Locate every blood parasite and identify its species.
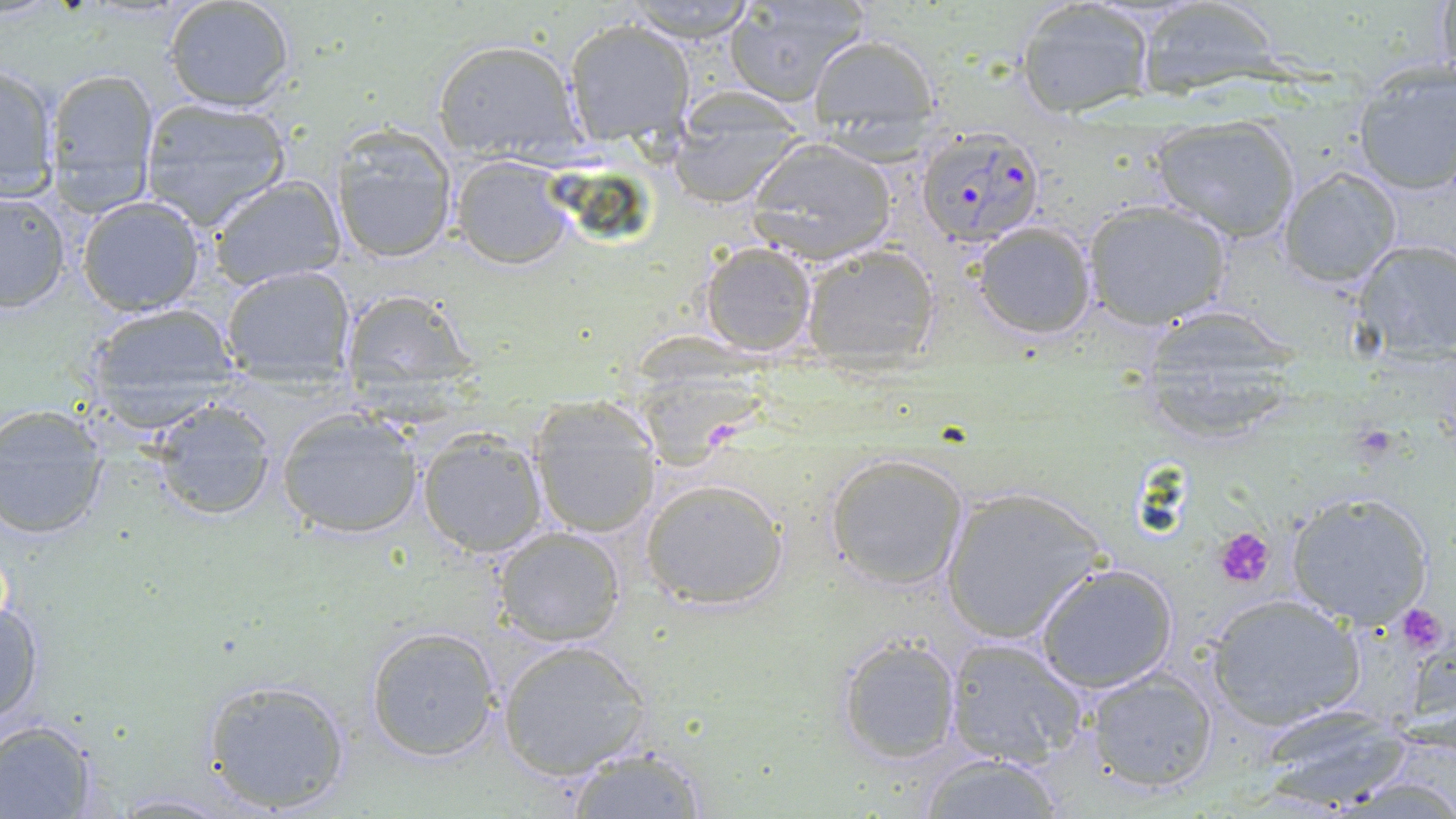

Approximate bounding boxes as named x1/y1/x2/y2 corners in pixels.
Plasmodium falciparum-infected red blood cells: (x1=915, y1=124, x2=1045, y2=250).
No Plasmodium ovale, Plasmodium malariae, Plasmodium vivax, Babesia divergens, or Trypanosoma brucei observed.

Summary:
  - Platelet locations: (x1=1213, y1=527, x2=1275, y2=589), (x1=1398, y1=605, x2=1449, y2=656)
  - Uninfected red blood cell locations: (x1=163, y1=0, x2=299, y2=113), (x1=617, y1=0, x2=761, y2=42), (x1=1133, y1=0, x2=1282, y2=100), (x1=1430, y1=0, x2=1455, y2=84), (x1=723, y1=1, x2=870, y2=107), (x1=1015, y1=1, x2=1155, y2=118), (x1=562, y1=20, x2=696, y2=142), (x1=807, y1=32, x2=940, y2=141), (x1=431, y1=37, x2=584, y2=160), (x1=1, y1=62, x2=60, y2=201), (x1=45, y1=68, x2=159, y2=207), (x1=1349, y1=77, x2=1455, y2=196), (x1=137, y1=96, x2=293, y2=229), (x1=1150, y1=115, x2=1302, y2=244), (x1=328, y1=124, x2=460, y2=265), (x1=668, y1=128, x2=797, y2=207), (x1=745, y1=140, x2=898, y2=264), (x1=449, y1=156, x2=575, y2=270), (x1=1277, y1=165, x2=1404, y2=288), (x1=206, y1=174, x2=346, y2=289), (x1=0, y1=189, x2=72, y2=313), (x1=75, y1=195, x2=208, y2=316), (x1=1078, y1=198, x2=1234, y2=329), (x1=970, y1=221, x2=1098, y2=341), (x1=1351, y1=239, x2=1456, y2=362), (x1=696, y1=241, x2=819, y2=358), (x1=801, y1=244, x2=941, y2=367), (x1=219, y1=265, x2=357, y2=387), (x1=339, y1=287, x2=479, y2=408), (x1=82, y1=304, x2=242, y2=428), (x1=1136, y1=312, x2=1309, y2=439), (x1=144, y1=396, x2=278, y2=525), (x1=528, y1=397, x2=663, y2=537), (x1=1, y1=402, x2=115, y2=542), (x1=274, y1=407, x2=426, y2=538), (x1=414, y1=427, x2=548, y2=559), (x1=823, y1=451, x2=971, y2=592), (x1=640, y1=477, x2=790, y2=609), (x1=938, y1=485, x2=1109, y2=646), (x1=1283, y1=489, x2=1436, y2=632), (x1=490, y1=525, x2=628, y2=647), (x1=1033, y1=562, x2=1179, y2=694), (x1=1202, y1=592, x2=1365, y2=731), (x1=1, y1=597, x2=46, y2=728), (x1=363, y1=625, x2=503, y2=763), (x1=833, y1=636, x2=963, y2=764), (x1=943, y1=636, x2=1091, y2=769), (x1=495, y1=637, x2=653, y2=779), (x1=1084, y1=668, x2=1220, y2=794), (x1=198, y1=677, x2=354, y2=814), (x1=1246, y1=703, x2=1423, y2=810), (x1=0, y1=720, x2=103, y2=818), (x1=563, y1=744, x2=711, y2=818), (x1=914, y1=754, x2=1074, y2=817)
  - Slide-level diagnosis: Plasmodium falciparum
  - Stain: May-Grünwald-Giemsa
  - Preparation: thin blood smear
  - Magnification: 1000x
  - Modality: optical microscopy
  - Field of view: one of a larger specimen
  - Image size: 1456×819 pixels